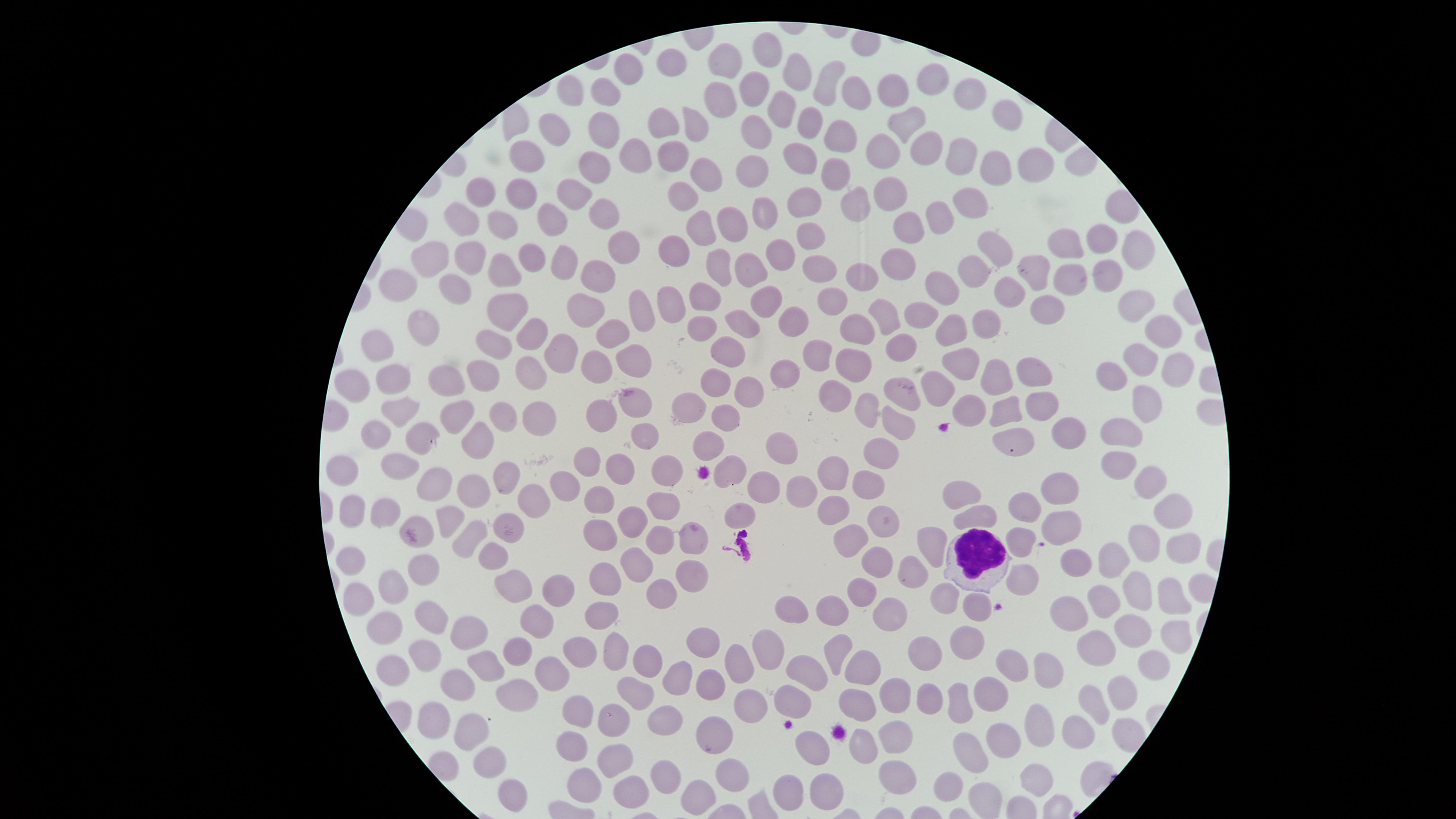
preparation = thin blood smear
uninfected red blood cells = approximate marker points as [x, y] in pixels: [768, 52], [675, 62], [728, 62], [631, 68], [795, 75], [933, 80], [829, 81], [753, 89], [855, 92], [896, 93], [973, 98], [608, 99], [719, 100], [783, 107], [1011, 112], [806, 122], [661, 123], [606, 124], [690, 126], [906, 127], [752, 131], [551, 133], [839, 137], [884, 145], [923, 147], [528, 152], [670, 155], [960, 155], [801, 156], [633, 159], [749, 165], [1029, 166], [837, 167], [997, 168], [593, 171], [706, 173], [520, 187], [478, 191], [893, 194], [685, 198], [573, 199], [804, 199], [856, 203], [975, 205], [770, 210], [940, 214], [602, 215], [464, 218], [554, 219], [730, 219], [507, 223], [911, 224], [699, 226], [810, 234], [1097, 239], [994, 243], [1068, 243], [1131, 247], [626, 249], [429, 250], [678, 250], [780, 250], [532, 259], [899, 259], [563, 261], [469, 262], [719, 264], [753, 264], [507, 268], [824, 268], [980, 269], [1038, 269], [1109, 272], [593, 276], [1068, 277], [859, 281], [406, 285], [454, 287], [940, 288], [1008, 293], [704, 298], [765, 299], [832, 300], [671, 307], [1143, 307], [506, 308], [1042, 308], [585, 311], [639, 312], [885, 313], [918, 315], [795, 319], [742, 324], [985, 325], [424, 326], [704, 327], [858, 327], [945, 327], [615, 328], [532, 331], [1161, 331], [494, 341], [901, 344], [378, 346], [559, 347], [725, 348], [635, 356], [813, 356], [593, 359], [1142, 359], [856, 361], [962, 365], [1180, 367], [1038, 368], [489, 371], [528, 374], [998, 374], [784, 376], [1115, 376], [396, 378], [355, 380], [448, 380], [715, 382], [750, 390], [940, 390], [836, 395], [906, 395], [631, 400], [1142, 400], [689, 404], [1034, 404], [1006, 406], [967, 408], [396, 410], [864, 410], [503, 412], [600, 412], [449, 413], [535, 415], [728, 415], [898, 423], [1120, 429], [380, 430], [645, 431], [1066, 434], [416, 435], [1011, 441], [480, 442], [708, 445], [882, 450], [777, 455], [586, 460], [1117, 464], [626, 465], [401, 466], [341, 467], [732, 468], [670, 470], [508, 473], [832, 474], [1145, 479], [865, 483], [439, 486], [566, 486], [478, 488], [766, 488], [1061, 488], [960, 492], [798, 493], [533, 498], [660, 503], [1026, 503], [602, 505], [833, 509], [738, 510], [985, 512], [353, 513], [385, 513], [1177, 514], [448, 515], [634, 519], [881, 519], [418, 521], [504, 523], [604, 532], [662, 536], [694, 536], [469, 537], [849, 537], [1141, 541], [1019, 543], [931, 545], [1183, 550], [498, 557], [351, 558], [1117, 559], [1078, 560], [876, 562], [636, 567], [692, 569], [425, 570], [601, 576], [910, 577], [1023, 581], [516, 582], [394, 586], [1136, 587], [557, 591], [660, 592], [1106, 592], [858, 595], [1171, 596], [361, 598], [945, 601], [1072, 605], [978, 606], [793, 607], [837, 610], [606, 614], [897, 616], [436, 620], [536, 621], [388, 624], [1133, 626], [472, 631], [1174, 631], [709, 643], [965, 643], [1100, 643], [617, 644], [513, 649], [924, 649], [425, 650], [833, 650], [577, 651], [641, 654], [766, 654], [734, 661], [490, 663], [390, 664], [1155, 664], [867, 665], [1010, 666], [1048, 667], [810, 669], [552, 675], [675, 676], [711, 679], [457, 682], [636, 689], [518, 690], [795, 691], [990, 691], [1122, 692], [897, 695], [928, 698], [1095, 699], [744, 702], [859, 704], [580, 707], [955, 707], [668, 714], [436, 719], [611, 720], [1043, 729], [1075, 729], [469, 731], [893, 733], [722, 734], [572, 741], [1000, 741], [865, 747], [810, 751], [974, 754], [495, 759], [617, 759], [898, 768], [732, 773], [673, 775], [585, 778], [1038, 778], [820, 782], [788, 788], [946, 788], [632, 790], [513, 793], [699, 794]
stain = Giemsa
image size = 1456×819 pixels
visible region = circular
presence = no malaria parasites detected
field of view = single
white blood cells = approximate marker points as [x, y] in pixels: [972, 558]
capture = smartphone photograph through the microscope eyepiece